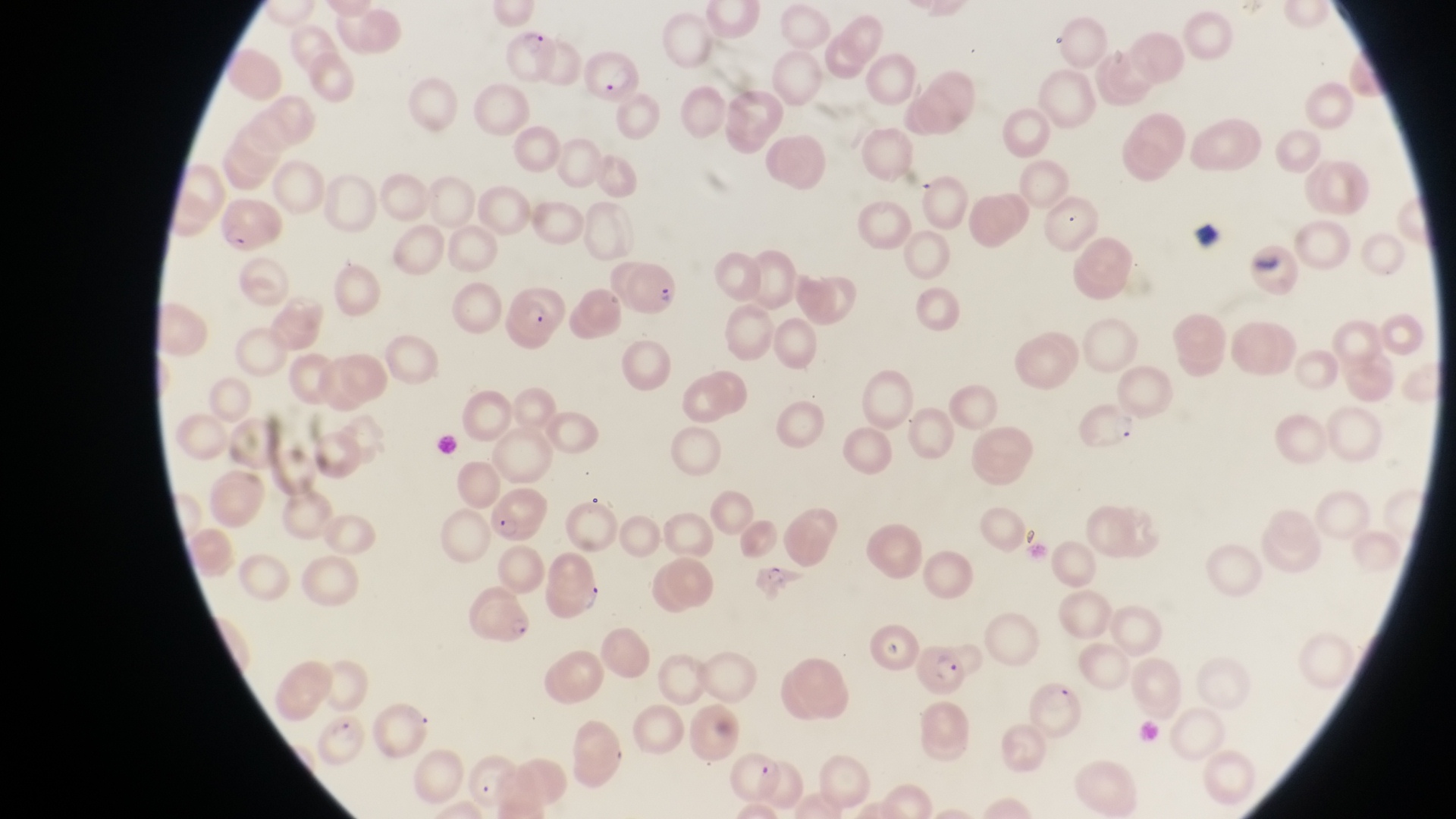
Approximate bounding boxes as {left, top, right, bottom} in pixels. Artifact (platelet-like body, stain precipitate, or debris) locations: {1194, 220, 1226, 251}, {1245, 245, 1282, 272}. Parasitised red blood cell locations: {499, 27, 557, 79}, {581, 50, 640, 106}, {217, 201, 281, 253}, {627, 265, 683, 312}, {497, 285, 568, 348}, {1070, 402, 1143, 457}, {483, 486, 542, 542}, {463, 589, 536, 647}, {915, 642, 968, 692}, {315, 708, 368, 766}. Thin blood smear. Magnification of 1000x. Captured by a smartphone held over the eyepiece of an Olympus CX-23 microscope. Image is 1456×819 pixels. One field of view. Sample from Uganda.